Classify this cell by malaria status.
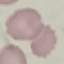
It is uninfected.

Summary:
  - Capture: smartphone camera at the microscope eyepiece
  - Image type: cell patch, automatically extracted from a larger field of view and resized to 64 × 64 pixels
  - Stain: Giemsa
  - Preparation: thin smear